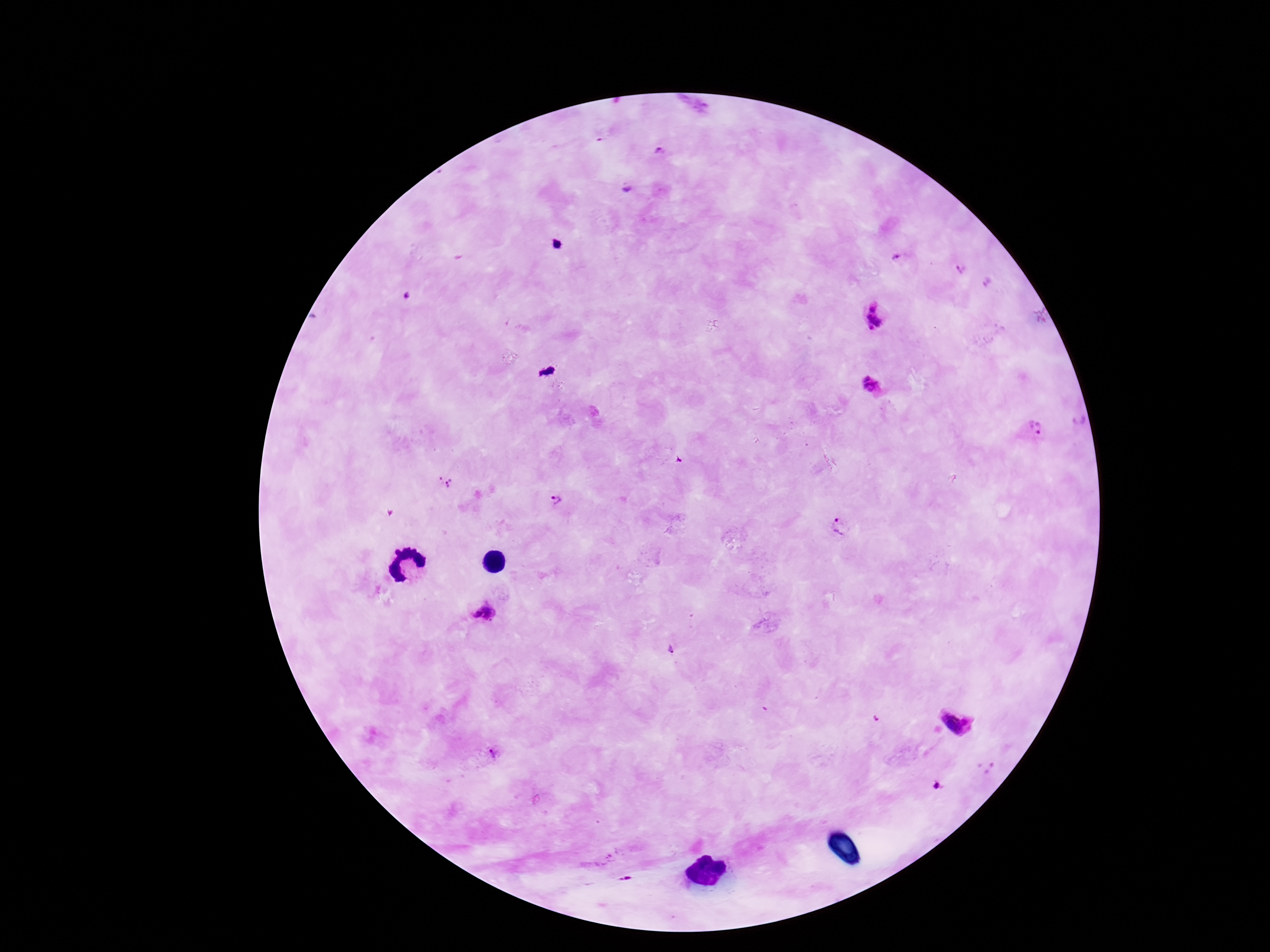
Approximate object centers, in pixels from the top-left corner.
Summary:
  - Plasmodium parasite locations: (x=660, y=154), (x=897, y=257), (x=961, y=268), (x=875, y=317), (x=869, y=383), (x=1036, y=427), (x=445, y=480), (x=556, y=500), (x=837, y=526), (x=486, y=612), (x=671, y=649), (x=959, y=718), (x=491, y=753), (x=938, y=786)
  - Preparation: thick peripheral-blood smear
  - Capture: smartphone camera through the microscope eyepiece
  - Patient malaria status: infected
  - Stain: Giemsa
  - Image size: 1270×952 pixels
  - Field of view: one from this slide
  - Magnification: 100x